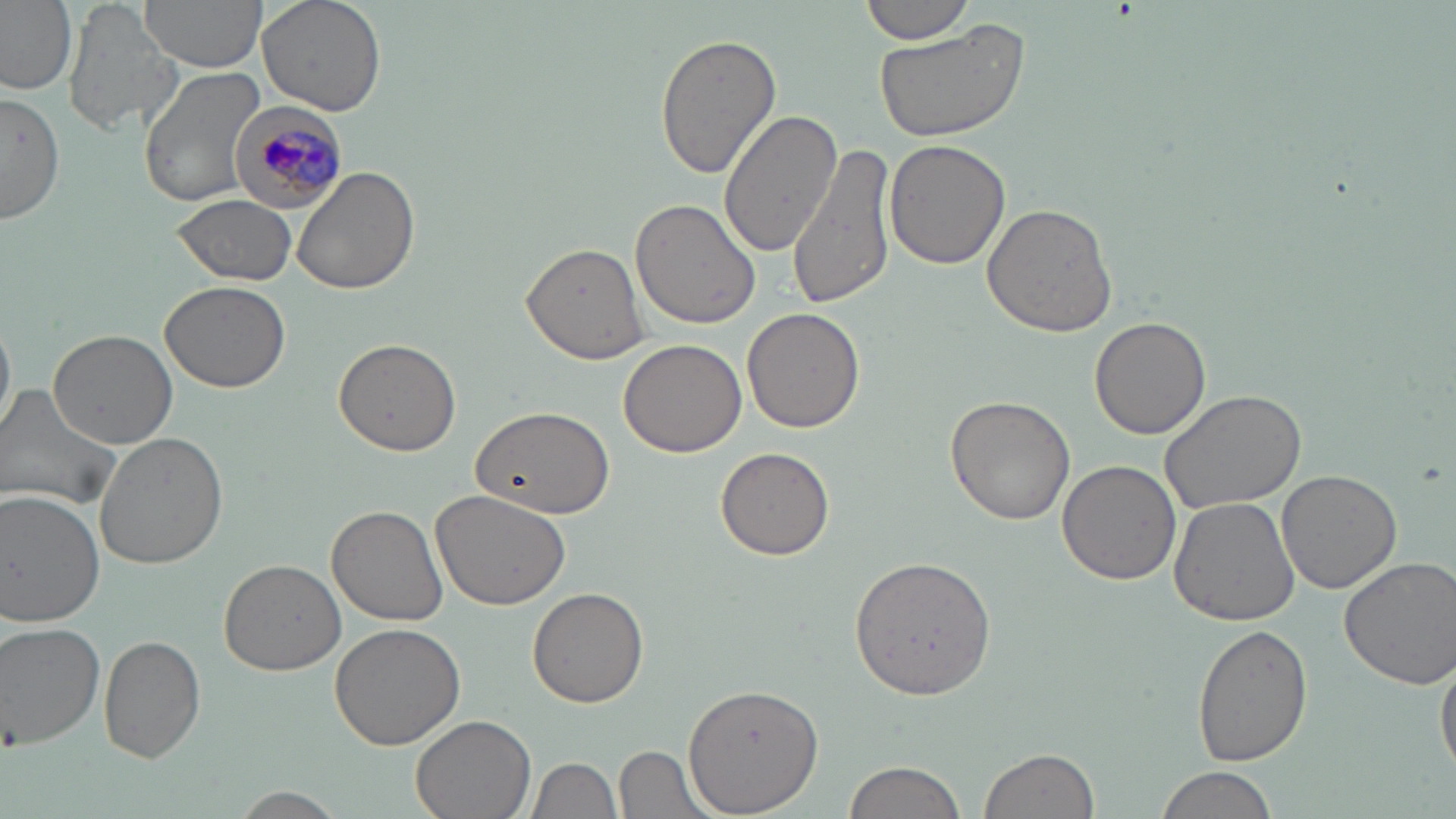
slide-level diagnosis = Plasmodium malariae
image size = 1456×819 pixels
stain = May-Grünwald-Giemsa
Plasmodium malariae-infected red blood cell locations = approximate bounding boxes as named x1/y1/x2/y2 corners in pixels: (x1=225, y1=100, x2=345, y2=214)
uninfected red blood cell locations = approximate bounding boxes as named x1/y1/x2/y2 corners in pixels: (x1=0, y1=0, x2=78, y2=97), (x1=141, y1=0, x2=265, y2=74), (x1=259, y1=0, x2=386, y2=116), (x1=860, y1=0, x2=978, y2=45), (x1=66, y1=4, x2=180, y2=138), (x1=871, y1=21, x2=1029, y2=147), (x1=74, y1=30, x2=217, y2=193), (x1=654, y1=32, x2=781, y2=182), (x1=138, y1=65, x2=264, y2=208), (x1=0, y1=89, x2=63, y2=228), (x1=719, y1=107, x2=840, y2=256), (x1=883, y1=139, x2=1010, y2=270), (x1=790, y1=140, x2=899, y2=309), (x1=291, y1=166, x2=422, y2=297), (x1=171, y1=193, x2=298, y2=285), (x1=631, y1=198, x2=764, y2=331), (x1=981, y1=204, x2=1117, y2=338), (x1=520, y1=242, x2=651, y2=366), (x1=159, y1=280, x2=293, y2=392), (x1=741, y1=308, x2=865, y2=434), (x1=0, y1=312, x2=15, y2=442), (x1=1090, y1=318, x2=1211, y2=440), (x1=48, y1=328, x2=179, y2=449), (x1=333, y1=338, x2=460, y2=457), (x1=619, y1=339, x2=747, y2=458), (x1=0, y1=384, x2=123, y2=515), (x1=1160, y1=387, x2=1309, y2=514), (x1=947, y1=393, x2=1077, y2=524), (x1=469, y1=404, x2=617, y2=519), (x1=93, y1=431, x2=228, y2=571), (x1=714, y1=447, x2=837, y2=561), (x1=1058, y1=461, x2=1182, y2=587), (x1=1277, y1=469, x2=1400, y2=593), (x1=431, y1=488, x2=571, y2=610), (x1=0, y1=491, x2=104, y2=627), (x1=1167, y1=497, x2=1300, y2=627), (x1=327, y1=505, x2=447, y2=625), (x1=851, y1=555, x2=995, y2=693), (x1=1337, y1=556, x2=1456, y2=689), (x1=219, y1=559, x2=346, y2=675), (x1=528, y1=587, x2=649, y2=709), (x1=1, y1=622, x2=106, y2=751), (x1=328, y1=623, x2=466, y2=751), (x1=1192, y1=623, x2=1309, y2=767), (x1=98, y1=635, x2=205, y2=762), (x1=1435, y1=649, x2=1456, y2=781), (x1=683, y1=685, x2=824, y2=811), (x1=409, y1=714, x2=536, y2=819), (x1=616, y1=745, x2=712, y2=817), (x1=978, y1=747, x2=1099, y2=819), (x1=527, y1=756, x2=622, y2=819), (x1=841, y1=759, x2=968, y2=819), (x1=1153, y1=766, x2=1277, y2=819), (x1=225, y1=789, x2=351, y2=819)
preparation = thin blood film
magnification = 1000x
modality = light microscopy
field of view = single